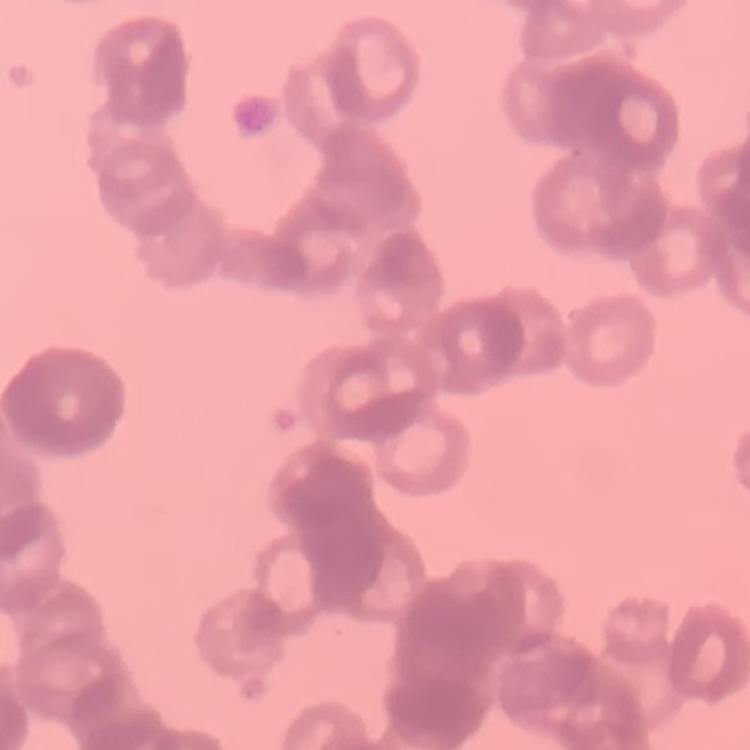
The red blood cells exhibit rouleaux formation. Thin blood smear. Field's or Giemsa stain. Square crop of a larger photomicrograph.